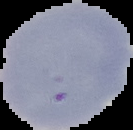
Summary:
  - Preparation: thin blood film
  - Result: no malaria parasites detected
  - Image type: cell region segmented out of the field of view; surrounding area masked to black
  - Image size: 133×130 pixels